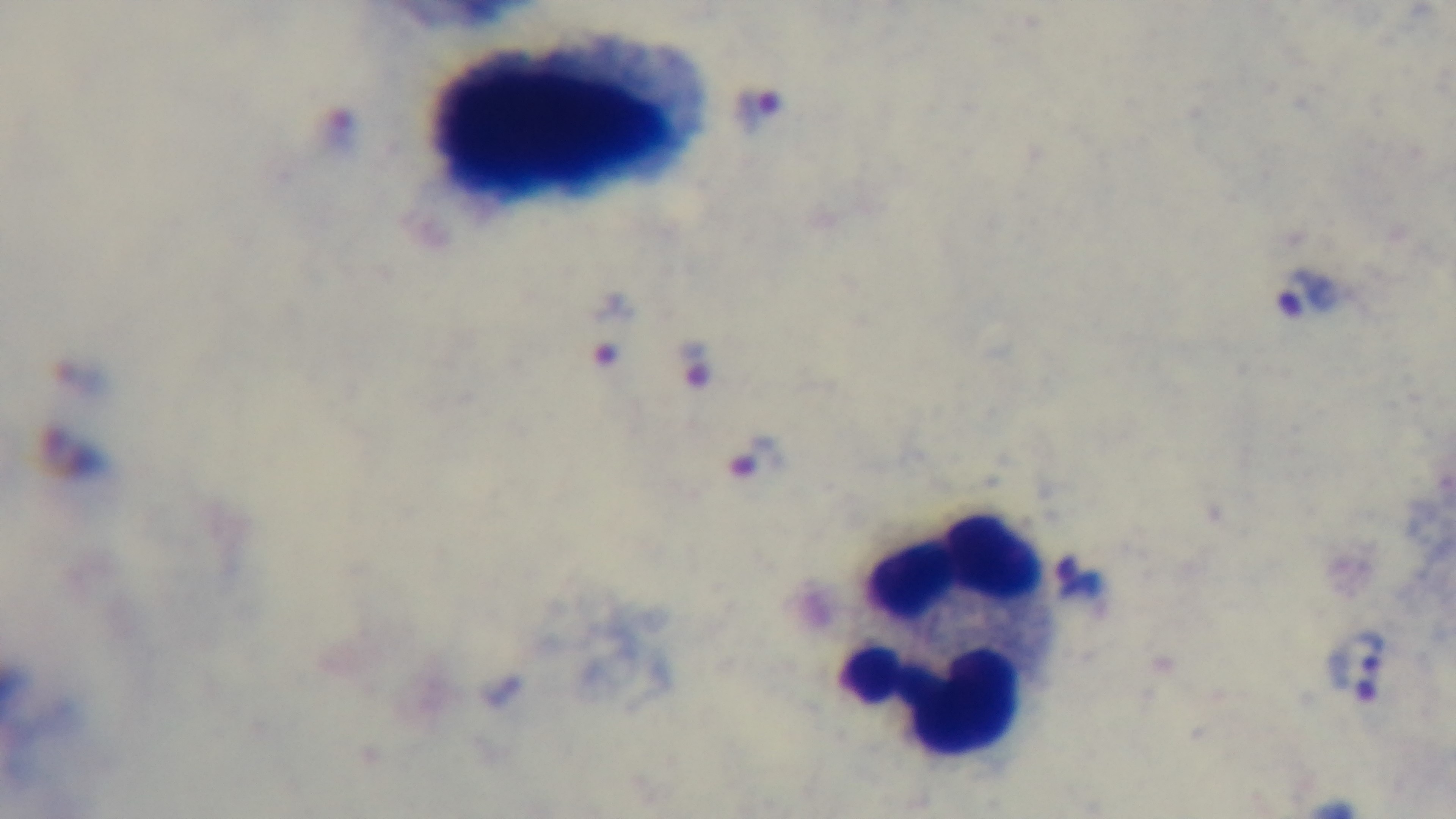
modality = light microscopy
capture = mounted 4K digital camera
objective = 100x oil immersion
field of view = single
malaria status = infected
preparation = thick
stain = Giemsa